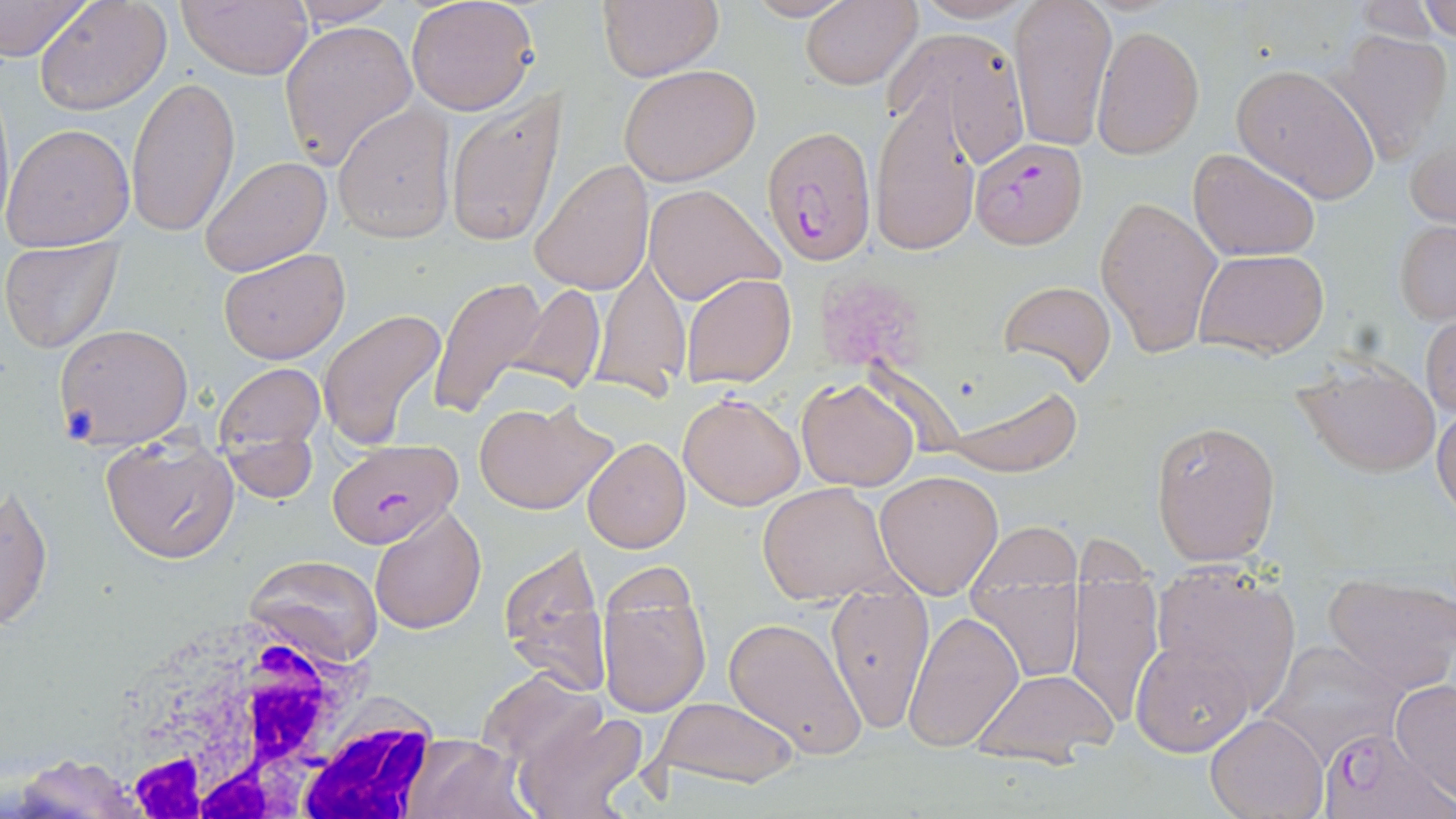
slide_level_diagnosis: Plasmodium falciparum
uninfected_red_blood_cell_locations: 'approximate bounding boxes as (x1, y1, x2, y2) in pixels: (0, 0, 95, 66), (34, 0, 173, 115), (284, 0, 404, 26), (407, 0, 540, 116), (595, 0, 723, 81), (740, 0, 857, 22), (908, 0, 1043, 24), (1007, 0, 1118, 150), (1348, 0, 1447, 42), (1417, 0, 1456, 42), (175, 1, 314, 79), (800, 1, 921, 90), (279, 19, 418, 170), (1091, 24, 1206, 159), (886, 25, 1030, 165), (1325, 27, 1455, 166), (618, 62, 763, 187), (1230, 64, 1380, 202), (126, 74, 240, 236), (0, 84, 15, 236), (870, 88, 982, 256), (444, 89, 565, 245), (332, 103, 456, 242), (1407, 120, 1455, 233), (1, 122, 134, 252), (1188, 147, 1321, 261), (199, 156, 331, 278), (530, 159, 655, 297), (644, 184, 783, 308), (1095, 193, 1222, 359), (1394, 218, 1456, 323), (1, 239, 122, 353), (219, 246, 350, 364), (1194, 249, 1330, 358), (593, 258, 691, 395), (680, 271, 796, 388), (427, 274, 547, 418), (996, 279, 1118, 390), (507, 281, 607, 395), (319, 308, 448, 454), (1420, 311, 1455, 418), (53, 323, 194, 447), (1288, 359, 1441, 477), (214, 362, 325, 477), (796, 377, 920, 490), (945, 380, 1082, 475), (678, 390, 805, 510), (472, 398, 617, 516), (1433, 404, 1456, 518), (1149, 418, 1282, 565), (99, 435, 240, 565), (583, 437, 691, 553), (875, 469, 1004, 598), (757, 483, 899, 604), (1, 485, 53, 634), (369, 504, 488, 632), (970, 522, 1083, 591), (497, 541, 611, 697), (243, 553, 385, 668), (970, 564, 1086, 685), (1149, 565, 1303, 712), (595, 568, 713, 720), (1063, 572, 1163, 730), (1322, 574, 1456, 695), (823, 584, 934, 730), (904, 610, 1025, 752), (723, 616, 870, 757), (1132, 637, 1257, 757), (1262, 641, 1408, 762), (969, 667, 1116, 763), (475, 670, 603, 772), (1391, 679, 1456, 802), (651, 695, 800, 790), (514, 705, 649, 819), (1205, 713, 1327, 819), (399, 734, 535, 819), (8, 754, 153, 819)'
field_of_view: one of a larger specimen
modality: light microscopy
platelet_locations: 'approximate bounding boxes as (x1, y1, x2, y2) in pixels: (818, 274, 917, 372)'
image_size: 1456×819 pixels
magnification: 1000x
white_blood_cell_locations: 'approximate bounding boxes as (x1, y1, x2, y2) in pixels: (79, 601, 456, 819)'
plasmodium_falciparum_infected_red_blood_cell_locations: 'approximate bounding boxes as (x1, y1, x2, y2) in pixels: (762, 126, 873, 265), (969, 138, 1087, 249), (325, 439, 462, 547), (1321, 726, 1447, 819)'
stain: May-Grünwald-Giemsa
preparation: thin blood smear